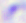

modality = photomicrograph
identification = Toxoplasma gondii
magnification = 400x